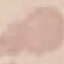

result = no malaria parasites detected
capture = smartphone through the microscope eyepiece
stain = Giemsa
image type = automatically extracted cell patch, resized to 64 × 64 pixels
preparation = thin smear